Give a bounding box for every Plasmodium parasite.
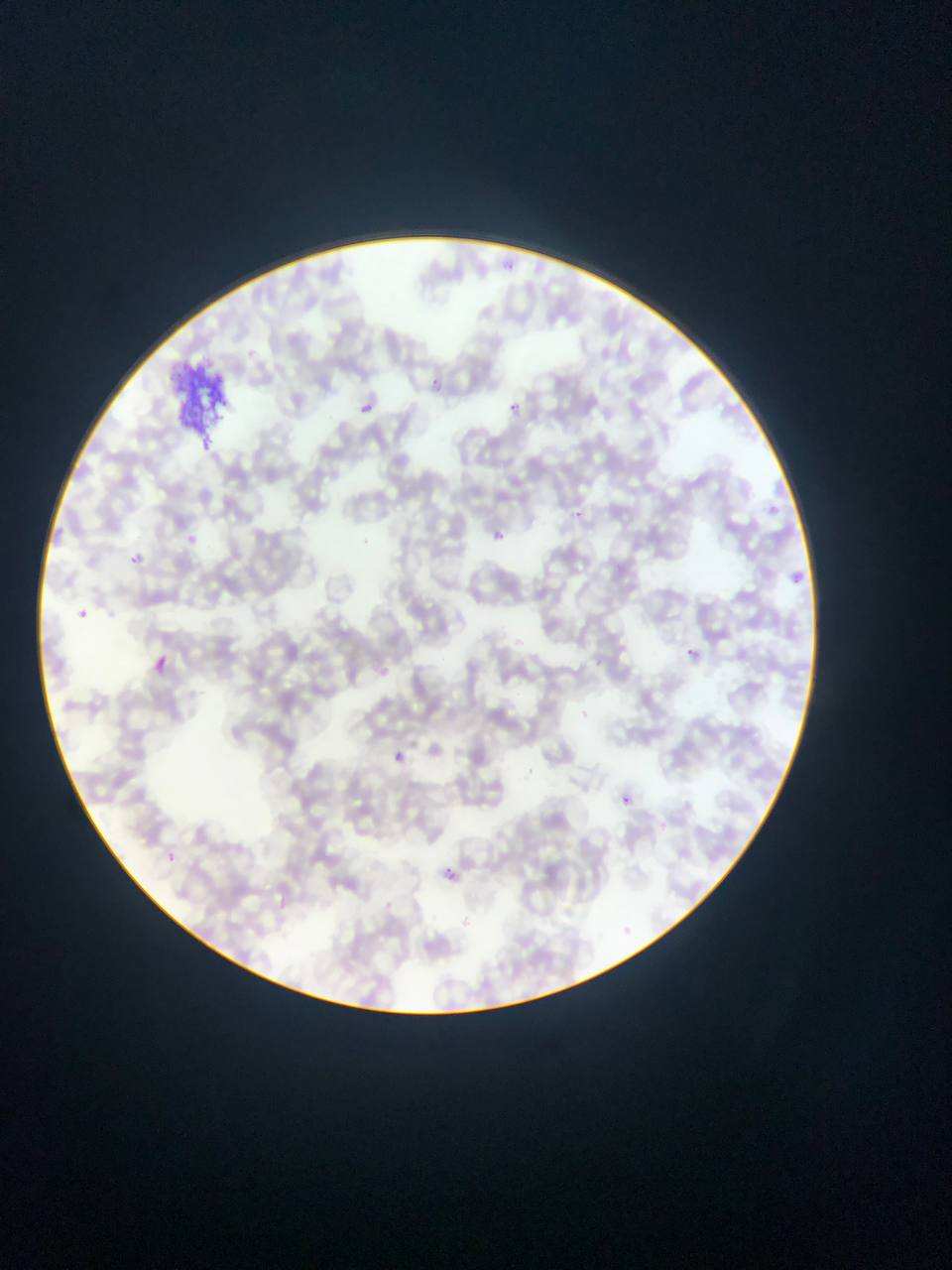
Approximate bounding boxes as [left, top, right, bottom] in pixels.
Plasmodium parasites: [497, 255, 527, 279], [431, 375, 451, 387], [361, 398, 383, 412], [510, 401, 535, 421], [771, 501, 780, 521], [572, 508, 594, 520], [489, 529, 506, 539], [182, 532, 195, 541], [131, 554, 141, 563], [788, 563, 813, 585], [76, 606, 102, 627], [684, 645, 703, 653], [156, 647, 181, 674], [388, 744, 403, 757], [617, 791, 640, 817], [440, 855, 484, 876].

Artifact (stain precipitate or debris) locations: [170, 352, 240, 443]. Photographed through a microscope with a mobile-phone camera. One field of view. Thin blood film. Sample from Ghana. Image is 952×1270 pixels.